Identify the cell.
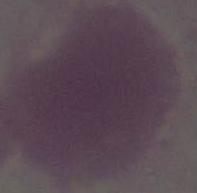
An erythrocyte.

Summary:
  - Magnification: 1000x
  - Modality: photomicrograph